Assess the morphology of the red blood cells.
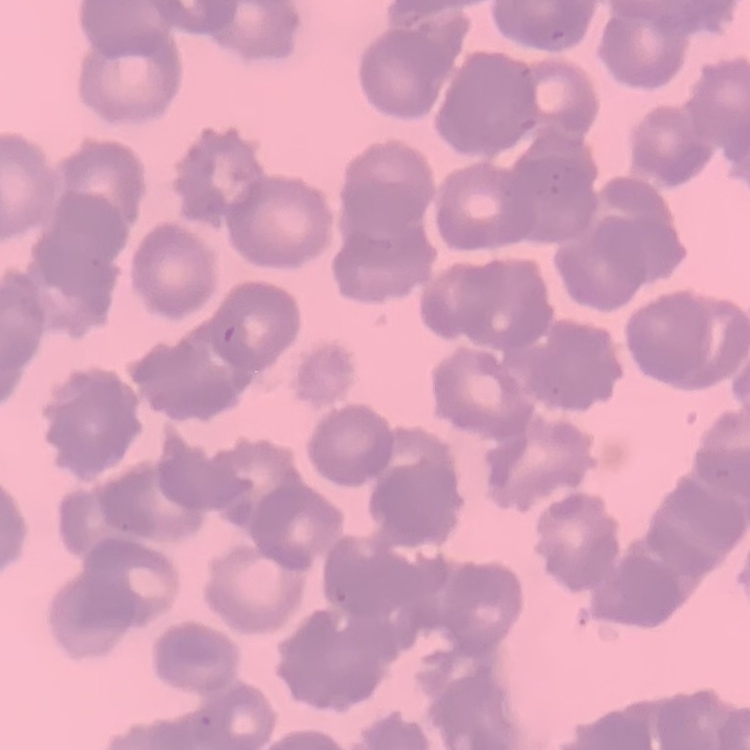
Rouleaux formation.

Thin blood smear. Square crop of a larger photomicrograph. Field's or Giemsa stain.